Look for Plasmodium parasites.
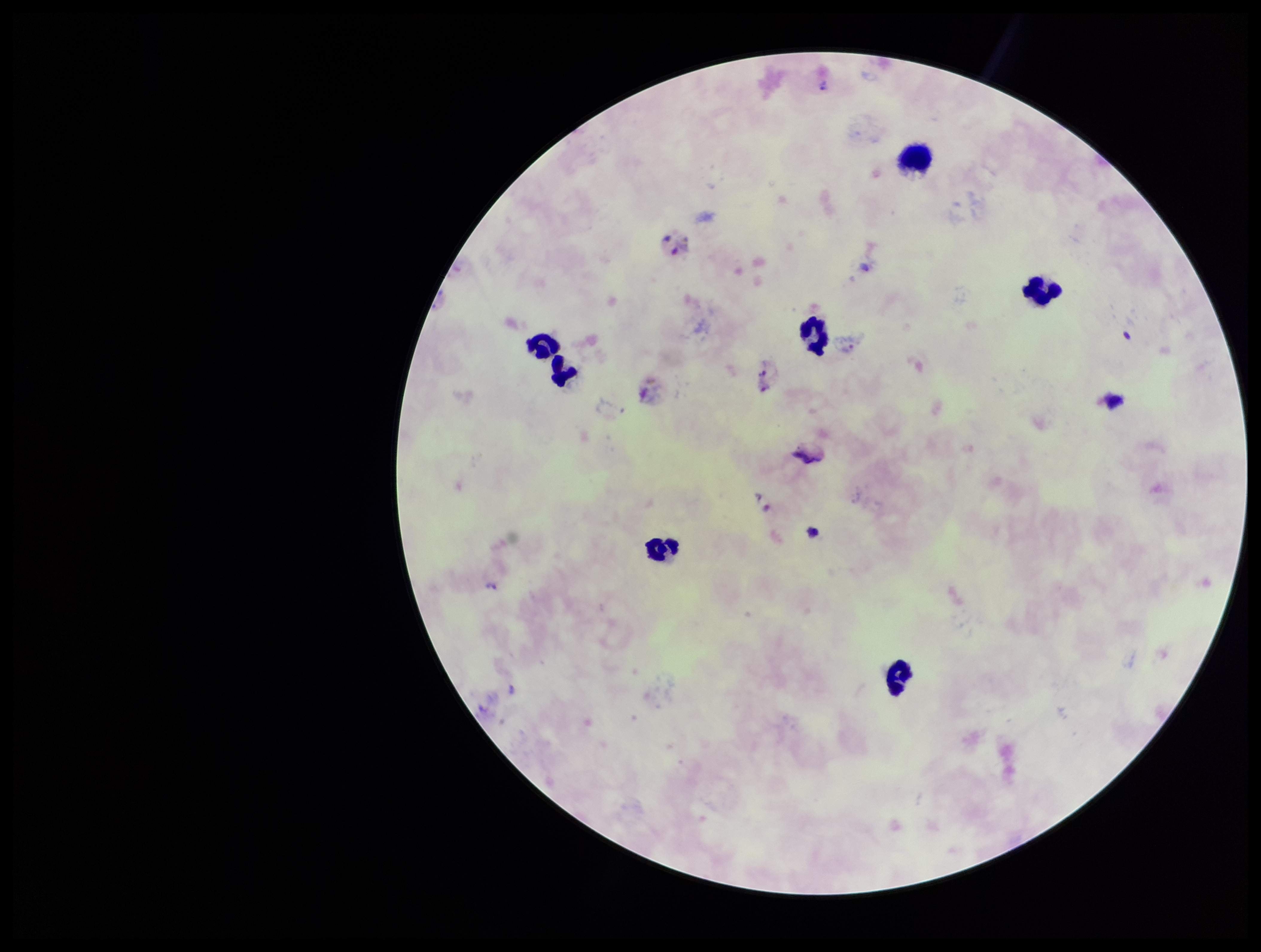
Identified.

Preparation: thick smear. One field from this slide. Leukocyte count: 7. Species reported for this patient: Plasmodium vivax. Smartphone photograph taken through the eyepiece of a microscope. Giemsa stain. Patient malaria status: positive. Parasite count: 6. Image is 1261×952 pixels.